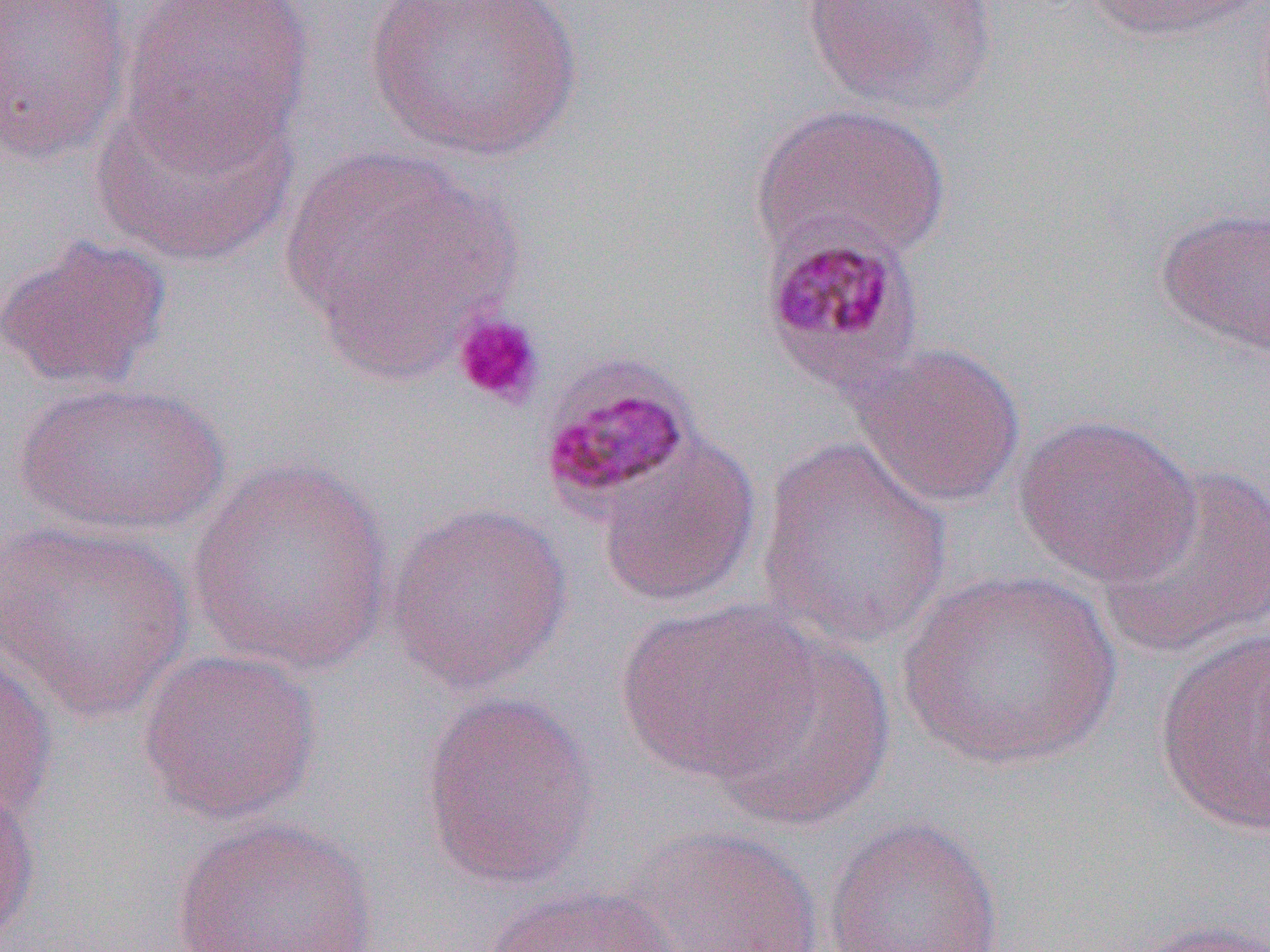
Summary:
  - Coordinate format: approximate bounding boxes as (x1,y1)-(x2,y2) corner pairs in pixels
  - Uninfected red blood cell locations: (0,0)-(133,167), (118,0)-(314,166), (363,0)-(582,163), (800,0)-(999,119), (1080,0)-(1265,42), (89,85)-(299,266), (751,102)-(951,266), (276,144)-(522,374), (1154,203)-(1270,359), (0,233)-(173,393), (852,341)-(1026,509), (11,379)-(230,539), (1014,413)-(1200,587), (755,433)-(955,653), (595,435)-(762,609), (186,460)-(395,674), (1097,461)-(1270,660), (383,499)-(575,695), (0,519)-(197,722), (896,569)-(1124,774), (615,598)-(820,785), (1153,625)-(1270,836), (703,633)-(896,831), (0,646)-(58,829), (135,647)-(322,826), (418,690)-(601,890), (0,780)-(41,945), (170,815)-(381,952), (823,815)-(1005,952), (629,825)-(826,952), (481,884)-(687,952), (1122,918)-(1270,952)
  - Platelet locations: (451,309)-(546,410)
  - Plasmodium malariae-infected red blood cell locations: (758,223)-(926,401), (535,351)-(701,519)
  - Slide-level diagnosis: Plasmodium malariae
  - Modality: light microscopy
  - Field of view: single
  - Image size: 1270×952 pixels
  - Preparation: thin blood film
  - Magnification: 1000x